Report the malaria status of this cell.
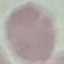
It is uninfected.

{
  "capture": "smartphone through the microscope eyepiece",
  "preparation": "thin smear",
  "image_type": "automatically extracted cell patch, resized to 64 × 64 pixels",
  "stain": "Giemsa"
}